Identify the cell.
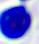

This is a leukocyte.

Summary:
  - Magnification: 400x
  - Modality: micrograph